Point out leukocytes.
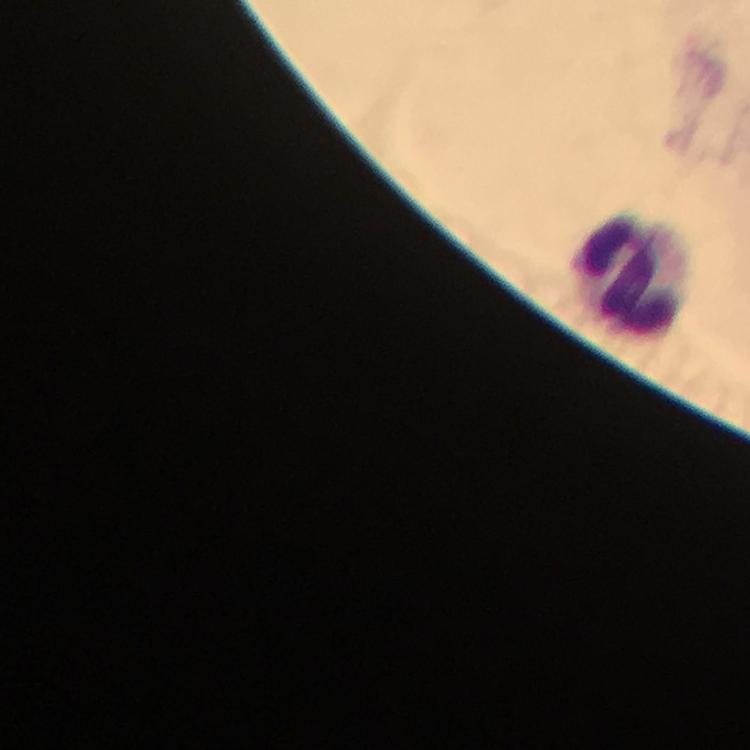
Approximate centers as {x, y} in pixels.
Leukocytes: {634, 275}.

immersion oil = used
preparation = thick blood film
Plasmodium parasites = none detected
cropped from = a single field of view
image size = 750×750 pixels
context = from a malaria diagnostic workup
capture = smartphone camera through the microscope
stain = Giemsa
magnification = 100x